Classify this cell by malaria status.
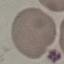

It is uninfected.

Acquired by smartphone through the microscope eyepiece. Thin smear of blood. Cell patch, automatically extracted from a larger field of view and resized to 64 × 64 pixels. Giemsa-stained preparation.